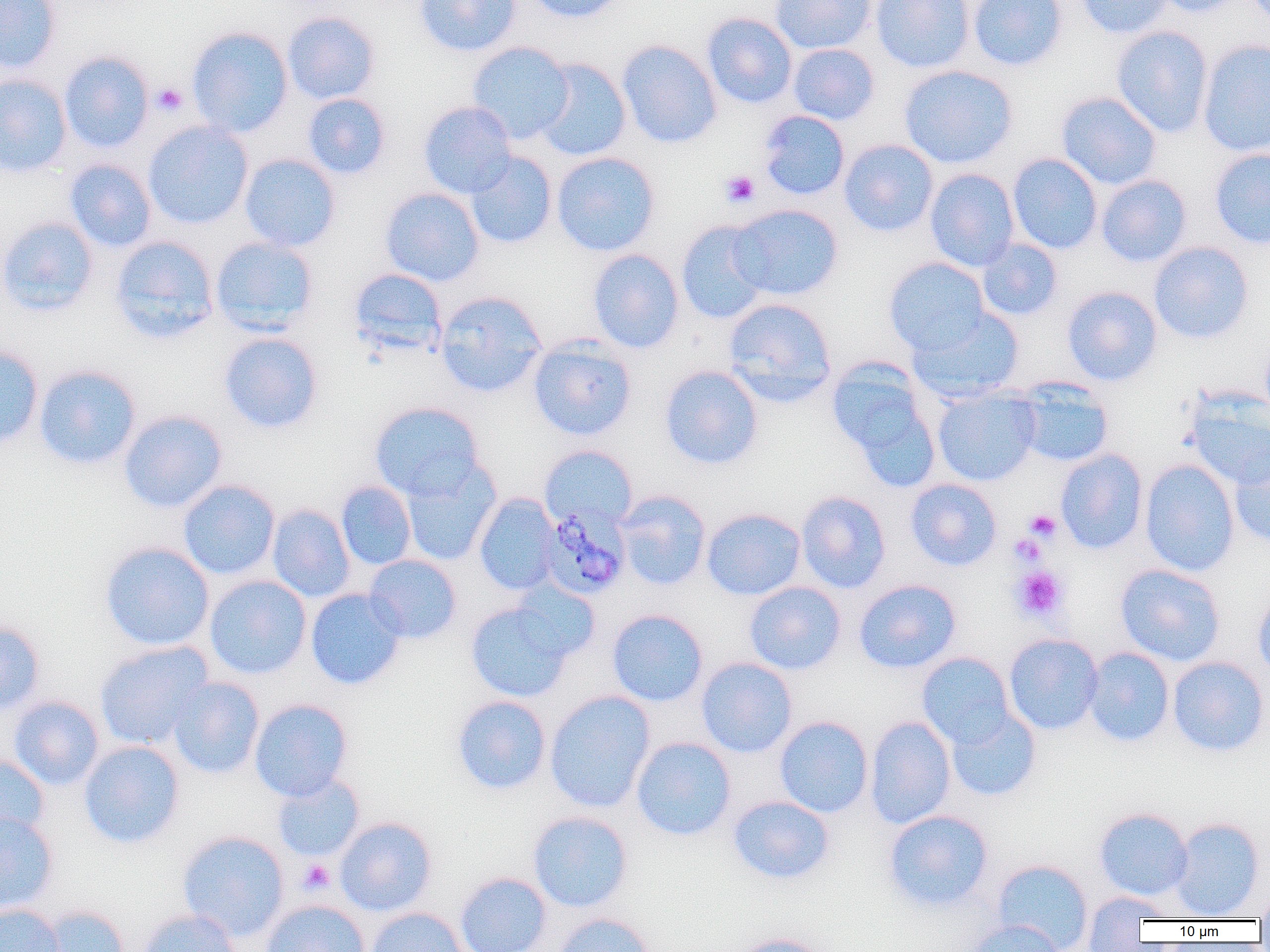
slide_level_diagnosis: Plasmodium malariae
image_size: 1270×952 pixels
magnification: 1000x
plasmodium_malariae_infected_red_blood_cell_locations: 'approximate bounding boxes as named x1/y1/x2/y2 corners in pixels: (x1=538, y1=504, x2=631, y2=600)'
preparation: thin blood smear
modality: optical microscopy
uninfected_red_blood_cell_locations: 'approximate bounding boxes as named x1/y1/x2/y2 corners in pixels: (x1=0, y1=0, x2=62, y2=74), (x1=414, y1=0, x2=522, y2=56), (x1=527, y1=0, x2=628, y2=23), (x1=770, y1=0, x2=876, y2=54), (x1=871, y1=0, x2=974, y2=73), (x1=968, y1=0, x2=1068, y2=71), (x1=1074, y1=0, x2=1174, y2=39), (x1=1150, y1=0, x2=1249, y2=17), (x1=282, y1=11, x2=380, y2=104), (x1=702, y1=13, x2=797, y2=108), (x1=1111, y1=25, x2=1213, y2=138), (x1=187, y1=26, x2=293, y2=138), (x1=1198, y1=39, x2=1270, y2=157), (x1=617, y1=40, x2=722, y2=148), (x1=467, y1=41, x2=574, y2=144), (x1=788, y1=43, x2=880, y2=125), (x1=58, y1=52, x2=154, y2=153), (x1=534, y1=58, x2=631, y2=161), (x1=898, y1=65, x2=1018, y2=168), (x1=0, y1=74, x2=72, y2=177), (x1=1056, y1=91, x2=1162, y2=190), (x1=303, y1=93, x2=390, y2=179), (x1=418, y1=101, x2=517, y2=198), (x1=757, y1=110, x2=850, y2=200), (x1=143, y1=122, x2=253, y2=229), (x1=839, y1=139, x2=939, y2=237), (x1=1209, y1=148, x2=1270, y2=249), (x1=465, y1=152, x2=557, y2=248), (x1=551, y1=152, x2=660, y2=257), (x1=239, y1=153, x2=340, y2=251), (x1=1007, y1=153, x2=1103, y2=254), (x1=64, y1=159, x2=157, y2=252), (x1=925, y1=168, x2=1019, y2=271), (x1=1096, y1=175, x2=1192, y2=267), (x1=379, y1=187, x2=484, y2=286), (x1=729, y1=204, x2=844, y2=301), (x1=0, y1=216, x2=99, y2=316), (x1=675, y1=220, x2=772, y2=324), (x1=110, y1=235, x2=220, y2=344), (x1=210, y1=237, x2=319, y2=335), (x1=976, y1=238, x2=1063, y2=321), (x1=1148, y1=241, x2=1254, y2=344), (x1=587, y1=249, x2=685, y2=354), (x1=883, y1=257, x2=989, y2=354), (x1=349, y1=268, x2=447, y2=357), (x1=1061, y1=286, x2=1163, y2=386), (x1=433, y1=290, x2=548, y2=397), (x1=722, y1=297, x2=837, y2=406), (x1=908, y1=307, x2=1025, y2=402), (x1=219, y1=332, x2=323, y2=433), (x1=528, y1=338, x2=637, y2=440), (x1=0, y1=345, x2=44, y2=449), (x1=827, y1=359, x2=942, y2=485), (x1=34, y1=365, x2=141, y2=469), (x1=659, y1=365, x2=764, y2=469), (x1=1014, y1=379, x2=1114, y2=468), (x1=932, y1=387, x2=1041, y2=486), (x1=1185, y1=390, x2=1270, y2=489), (x1=369, y1=401, x2=485, y2=501), (x1=119, y1=410, x2=227, y2=513), (x1=540, y1=445, x2=638, y2=530), (x1=1229, y1=445, x2=1270, y2=547), (x1=1055, y1=449, x2=1148, y2=554), (x1=400, y1=458, x2=501, y2=566), (x1=1139, y1=459, x2=1240, y2=577), (x1=905, y1=478, x2=1002, y2=571), (x1=178, y1=480, x2=280, y2=580), (x1=336, y1=481, x2=416, y2=570), (x1=615, y1=490, x2=711, y2=590), (x1=796, y1=491, x2=891, y2=593), (x1=474, y1=493, x2=561, y2=596), (x1=267, y1=504, x2=355, y2=602), (x1=701, y1=508, x2=806, y2=600), (x1=99, y1=542, x2=215, y2=651), (x1=363, y1=554, x2=462, y2=644), (x1=1115, y1=563, x2=1226, y2=666), (x1=204, y1=575, x2=311, y2=679), (x1=853, y1=579, x2=962, y2=673), (x1=744, y1=581, x2=846, y2=675), (x1=305, y1=588, x2=407, y2=690), (x1=1253, y1=588, x2=1270, y2=682), (x1=465, y1=599, x2=577, y2=702), (x1=607, y1=608, x2=708, y2=707), (x1=0, y1=620, x2=45, y2=715), (x1=1003, y1=633, x2=1104, y2=735), (x1=94, y1=641, x2=214, y2=750), (x1=1083, y1=647, x2=1175, y2=747), (x1=916, y1=652, x2=1015, y2=747), (x1=1167, y1=656, x2=1270, y2=757), (x1=696, y1=657, x2=797, y2=758), (x1=168, y1=677, x2=265, y2=779), (x1=545, y1=690, x2=656, y2=813), (x1=9, y1=695, x2=104, y2=790), (x1=451, y1=695, x2=552, y2=795), (x1=249, y1=698, x2=352, y2=802), (x1=945, y1=707, x2=1042, y2=801), (x1=864, y1=715, x2=956, y2=829), (x1=774, y1=716, x2=873, y2=818), (x1=631, y1=737, x2=737, y2=841), (x1=79, y1=741, x2=185, y2=848), (x1=0, y1=754, x2=49, y2=843), (x1=272, y1=774, x2=364, y2=862), (x1=728, y1=795, x2=835, y2=884), (x1=1093, y1=807, x2=1194, y2=900), (x1=882, y1=809, x2=994, y2=912), (x1=527, y1=811, x2=633, y2=912), (x1=0, y1=813, x2=59, y2=914), (x1=335, y1=817, x2=437, y2=916), (x1=1168, y1=817, x2=1265, y2=919), (x1=177, y1=831, x2=289, y2=941), (x1=991, y1=859, x2=1093, y2=951), (x1=454, y1=872, x2=552, y2=952), (x1=1254, y1=888, x2=1270, y2=924), (x1=1082, y1=890, x2=1172, y2=946), (x1=261, y1=899, x2=370, y2=952), (x1=0, y1=903, x2=65, y2=952), (x1=37, y1=905, x2=129, y2=952), (x1=365, y1=907, x2=469, y2=952), (x1=138, y1=908, x2=243, y2=952), (x1=553, y1=912, x2=656, y2=952), (x1=967, y1=919, x2=1066, y2=952), (x1=727, y1=933, x2=830, y2=952)'
platelet_locations: 'approximate bounding boxes as named x1/y1/x2/y2 corners in pixels: (x1=151, y1=83, x2=187, y2=116), (x1=720, y1=170, x2=760, y2=208), (x1=1024, y1=509, x2=1062, y2=542), (x1=1014, y1=519, x2=1056, y2=555), (x1=1010, y1=532, x2=1045, y2=565), (x1=1012, y1=566, x2=1067, y2=621), (x1=298, y1=859, x2=335, y2=894)'
field_of_view: single